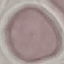

Result: negative for malaria parasites. Automatically extracted cell patch, resized to 64 × 64 pixels. Thin blood film. Giemsa-stained preparation. Photographed with a smartphone camera at the microscope eyepiece.